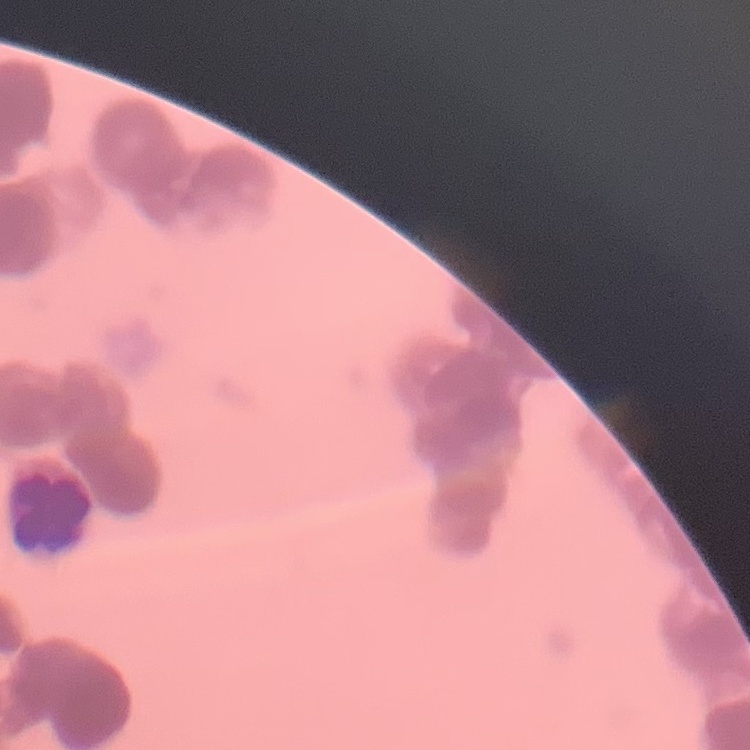

The red blood cells show rouleaux formation. Thin blood smear. One tile cut from a larger photomicrograph. Field's or Giemsa stain.